Assess the morphology of the erythrocytes.
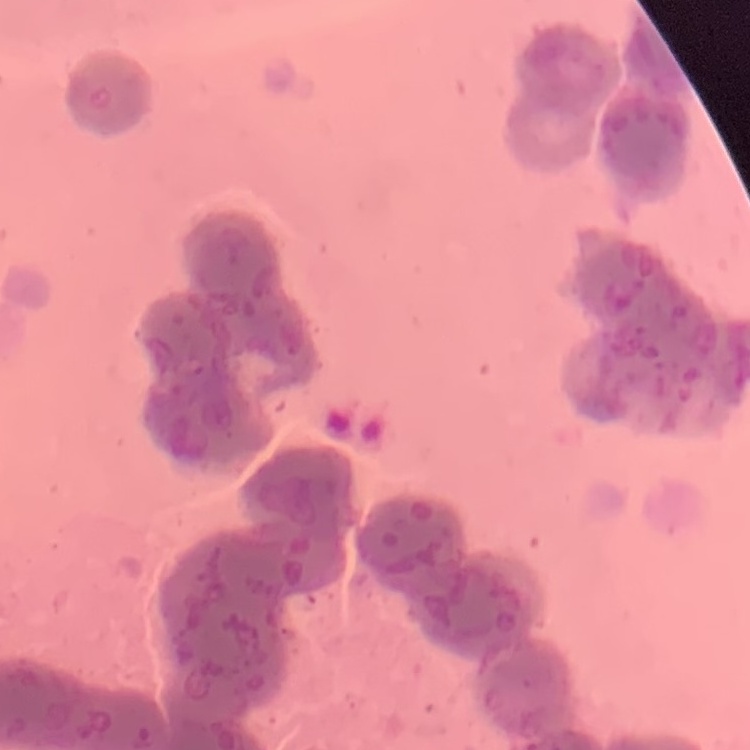
They show rouleaux formation.

{
  "image_type": "one tile cut from a larger photomicrograph",
  "preparation": "thin blood smear",
  "stain": "Field's or Giemsa"
}